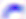

Micrograph. 400x magnification. Toxoplasma gondii is shown.